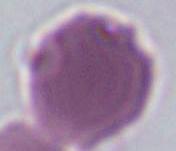

{
  "modality": "photomicrograph",
  "identification": "red blood cell",
  "magnification": "1000x"
}